Comment on the morphology of the red blood cells.
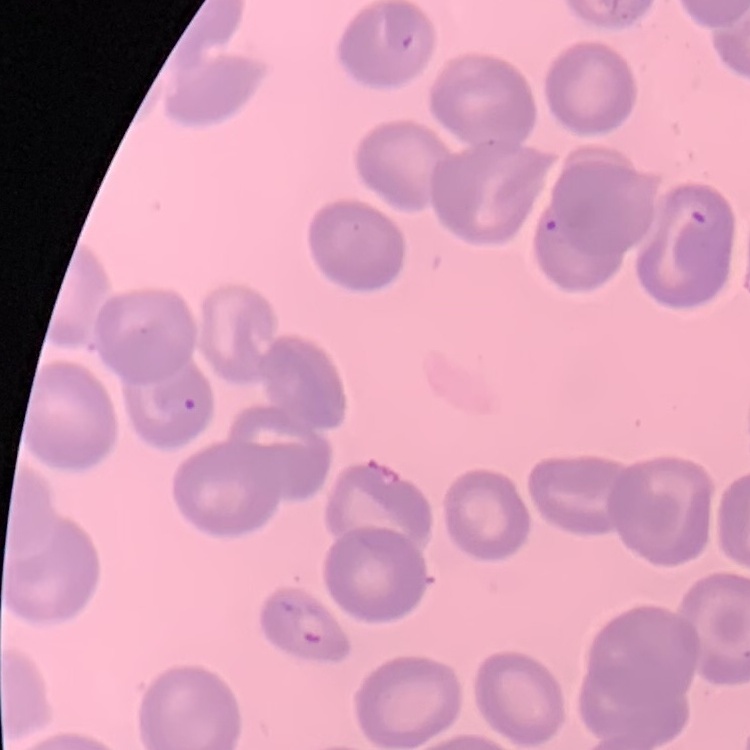
They show no rouleaux formation.

Thin peripheral smear. Stained with either Field's or Giemsa. One tile cut from a larger photomicrograph.